Name the parasite shown.
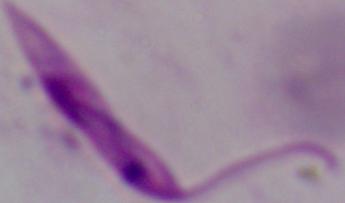
This is Leishmania.

{
  "magnification": "1000x",
  "modality": "photomicrograph"
}